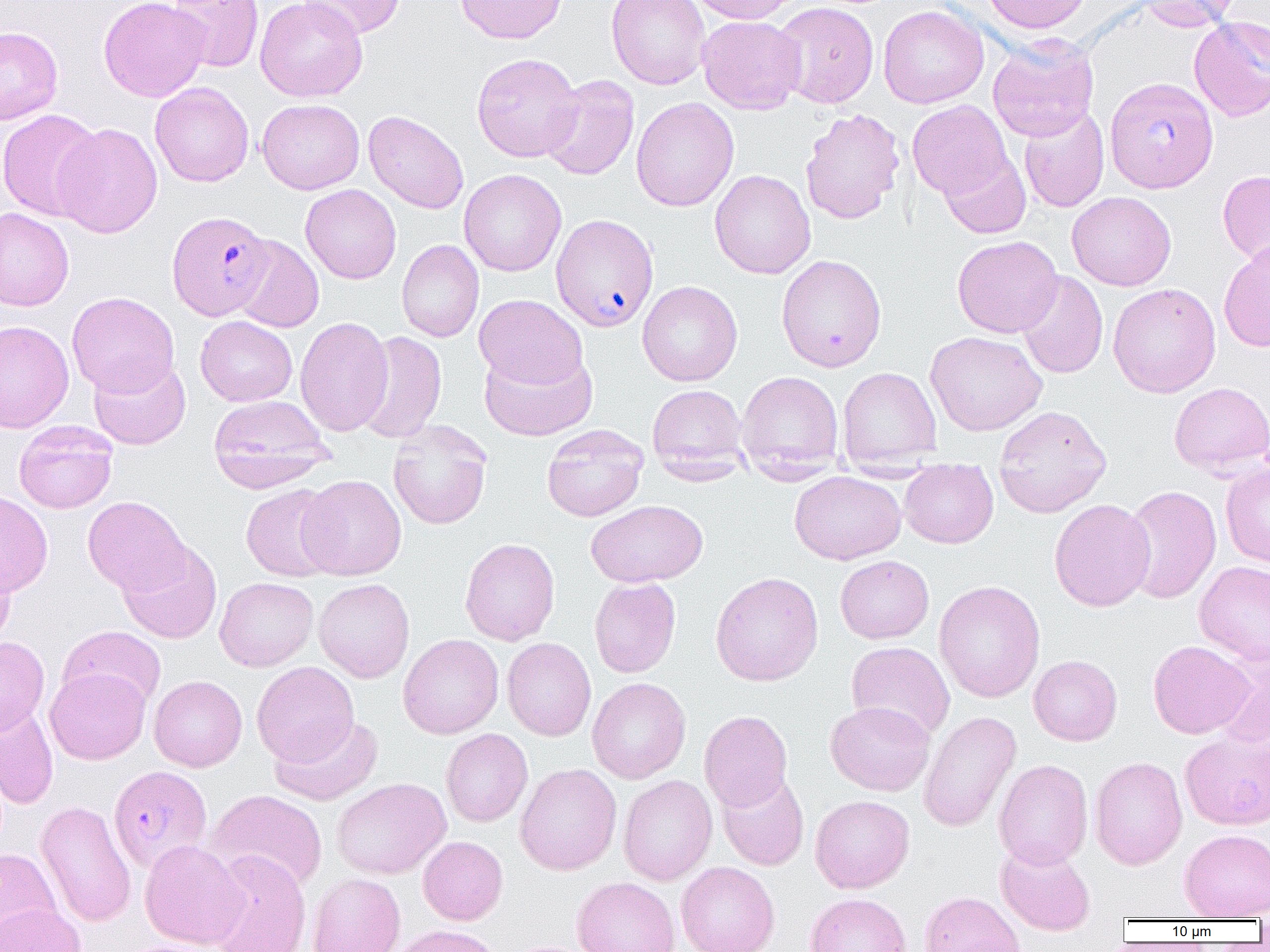
Approximate bounding boxes as (x1, y1, x2, y2) in pixels. Plasmodium falciparum-infected red blood cell locations: (1104, 76, 1219, 193), (167, 210, 274, 320), (551, 215, 659, 332), (113, 769, 217, 878). Uninfected red blood cell locations: (98, 0, 210, 102), (167, 0, 264, 72), (255, 0, 368, 102), (296, 0, 406, 40), (455, 0, 567, 44), (607, 0, 710, 90), (687, 0, 800, 24), (981, 0, 1093, 34), (1136, 0, 1240, 32), (772, 1, 879, 108), (878, 4, 989, 109), (697, 15, 806, 115), (1189, 16, 1270, 121), (0, 26, 63, 125), (987, 35, 1099, 141), (471, 52, 583, 162), (540, 75, 640, 181), (150, 82, 254, 187), (631, 97, 739, 211), (257, 98, 365, 194), (907, 100, 1013, 199), (1018, 105, 1110, 213), (800, 108, 905, 224), (0, 109, 104, 221), (363, 110, 469, 214), (52, 122, 163, 238), (939, 150, 1031, 239), (458, 169, 567, 276), (710, 169, 816, 279), (1218, 169, 1270, 268), (300, 184, 401, 284), (1067, 191, 1177, 291), (0, 208, 74, 312), (943, 233, 1053, 438), (952, 235, 1063, 338), (231, 236, 324, 333), (397, 240, 484, 342), (1218, 240, 1270, 353), (776, 254, 887, 372), (1016, 271, 1108, 379), (637, 280, 742, 386), (1107, 282, 1221, 398), (67, 292, 179, 397), (474, 294, 588, 390), (195, 316, 297, 406), (295, 316, 393, 436), (0, 320, 74, 434), (355, 330, 448, 443), (924, 330, 1047, 436), (479, 346, 597, 441), (88, 356, 191, 450), (837, 366, 942, 468), (736, 371, 844, 478), (1168, 382, 1270, 476), (647, 384, 749, 478), (208, 394, 333, 490), (993, 405, 1112, 518), (388, 420, 492, 530), (14, 421, 118, 514), (541, 425, 647, 522), (1220, 461, 1270, 568), (899, 462, 998, 548), (789, 471, 906, 564), (297, 474, 406, 580), (240, 483, 342, 582), (1121, 485, 1221, 604), (0, 490, 53, 598), (83, 496, 190, 595), (1049, 498, 1156, 612), (586, 500, 708, 587), (459, 538, 560, 646), (117, 540, 222, 643), (0, 553, 15, 650), (835, 555, 934, 643), (1194, 561, 1270, 664), (710, 571, 824, 686), (215, 577, 318, 671), (313, 578, 415, 682), (589, 578, 681, 677), (933, 580, 1045, 703), (58, 625, 166, 711), (398, 633, 504, 739), (0, 637, 49, 735), (502, 637, 596, 741), (1147, 640, 1254, 739), (846, 642, 955, 741), (1210, 646, 1270, 749), (1028, 655, 1122, 746), (251, 661, 359, 766), (45, 667, 150, 764), (149, 675, 247, 772), (587, 677, 691, 784), (825, 701, 935, 796), (0, 704, 59, 809), (698, 710, 793, 812), (918, 711, 1021, 833), (270, 715, 383, 806), (441, 729, 533, 827), (1180, 730, 1270, 830), (1089, 756, 1187, 870), (993, 759, 1093, 869), (515, 763, 622, 875), (716, 772, 809, 871), (618, 775, 718, 885), (331, 777, 451, 879), (207, 789, 328, 893), (809, 795, 914, 893), (35, 800, 136, 927), (1179, 829, 1270, 920), (418, 836, 508, 925), (139, 839, 248, 949), (995, 842, 1096, 935), (0, 848, 61, 942), (205, 850, 311, 952), (676, 861, 779, 952), (307, 873, 405, 952), (571, 877, 680, 952), (919, 891, 1025, 952), (805, 892, 912, 952), (0, 902, 85, 952), (388, 924, 504, 952), (117, 938, 238, 952). Slide-level diagnosis: Plasmodium falciparum. Captured at 1000x magnification. Light microscopy. Image is 1270×952 pixels. Single field of view. Thin blood smear.